Assess the morphology of the red blood cells.
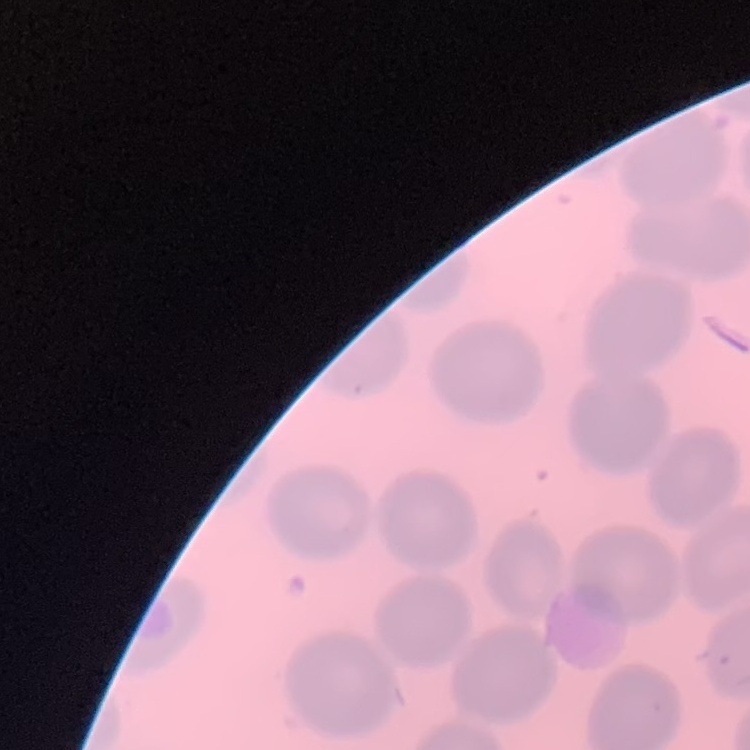

No rouleaux formation.

Stained with either Field's or Giemsa. One tile cut from a larger photomicrograph. Thin peripheral smear.